Locate every Plasmodium falciparum-infected red blood cell.
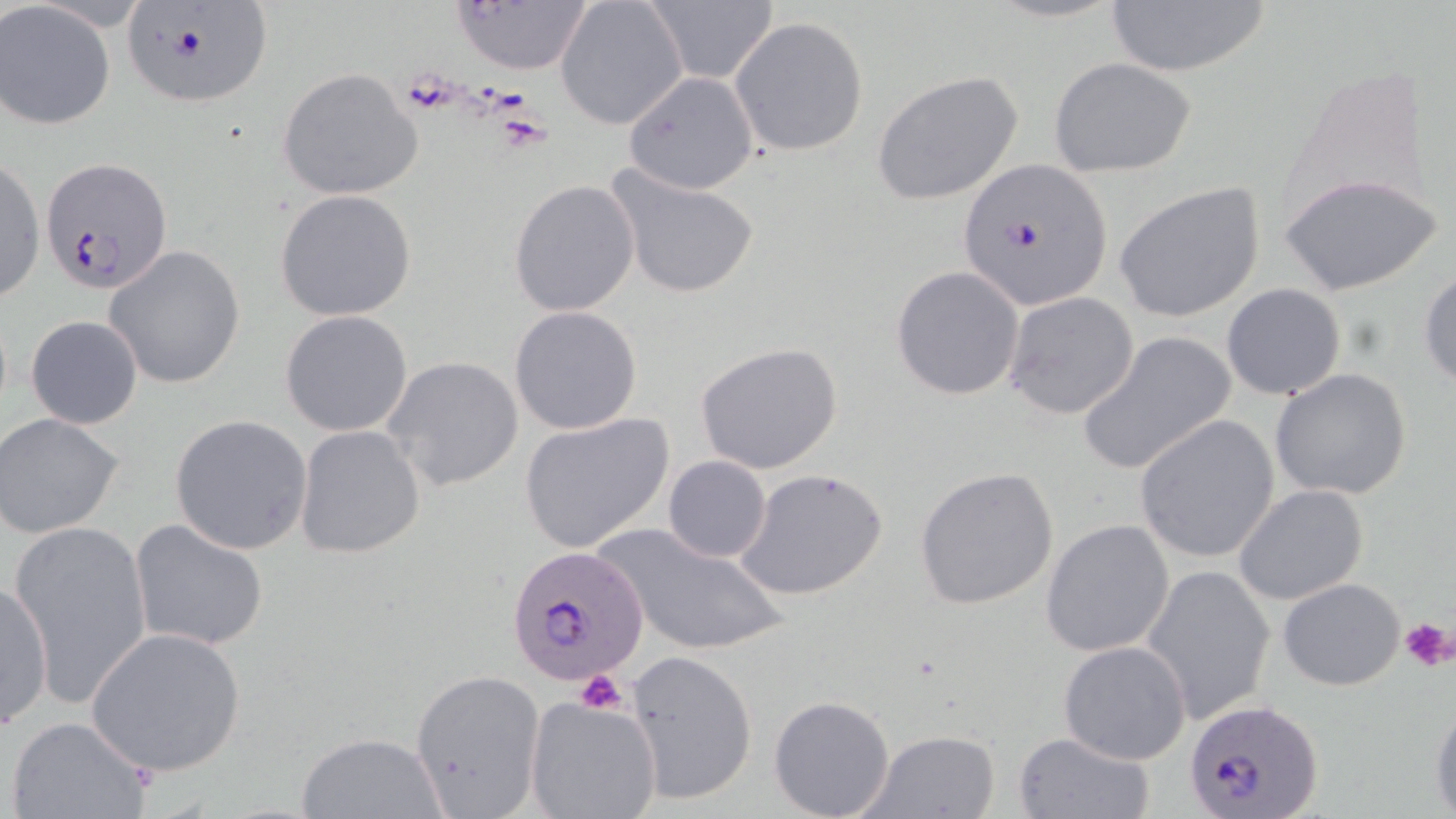

Approximate bounding boxes as (x1, y1, x2, y2) in pixels.
Plasmodium falciparum-infected red blood cells: (120, 4, 273, 109), (40, 159, 171, 295), (959, 160, 1112, 312), (505, 542, 651, 687), (1188, 700, 1325, 818).

Summary:
  - Uninfected red blood cell locations: (555, 0, 688, 130), (643, 1, 779, 85), (1104, 1, 1274, 78), (452, 2, 594, 76), (0, 3, 115, 130), (730, 17, 871, 158), (1047, 56, 1195, 177), (277, 68, 423, 200), (871, 69, 1025, 206), (622, 70, 760, 194), (1, 155, 46, 307), (609, 167, 760, 300), (1279, 171, 1444, 296), (509, 179, 641, 319), (1115, 181, 1266, 324), (275, 188, 420, 322), (104, 244, 246, 389), (1418, 264, 1456, 388), (890, 266, 1024, 400), (1221, 284, 1347, 400), (1003, 292, 1140, 419), (509, 305, 642, 434), (280, 310, 414, 436), (25, 315, 143, 429), (1077, 331, 1236, 477), (694, 341, 844, 474), (382, 355, 523, 491), (1270, 368, 1412, 501), (517, 412, 674, 553), (169, 413, 314, 555), (1, 414, 125, 539), (1134, 415, 1281, 565), (293, 425, 425, 559), (662, 455, 771, 564), (735, 465, 889, 602), (913, 467, 1061, 610), (1233, 484, 1370, 606), (129, 518, 271, 653), (1041, 518, 1175, 657), (8, 521, 154, 708), (601, 524, 785, 656), (1140, 563, 1277, 725), (1278, 576, 1406, 690), (0, 581, 54, 731), (84, 625, 247, 779), (1058, 639, 1191, 765), (626, 648, 758, 808), (409, 668, 545, 813), (767, 694, 895, 818), (523, 695, 661, 819), (1428, 697, 1456, 815), (5, 715, 154, 819), (860, 728, 1001, 817), (297, 730, 447, 818), (1012, 731, 1154, 818)
  - Platelet locations: (401, 70, 460, 111), (494, 111, 551, 148), (1400, 615, 1455, 672), (574, 670, 629, 714)
  - Slide-level diagnosis: Plasmodium falciparum
  - Magnification: 1000x
  - Image size: 1456×819 pixels
  - Field of view: single
  - Modality: optical microscopy
  - Preparation: thin blood film
  - Stain: May-Grünwald-Giemsa